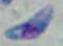

{
  "identification": "Toxoplasma gondii",
  "magnification": "1000x",
  "modality": "micrograph"
}